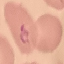

Result: malaria parasites identified. Photographed with a smartphone camera at the microscope eyepiece. Thin blood film. Cell patch, automatically extracted from a larger field of view and resized to 64 × 64 pixels. Giemsa-stained preparation.